Locate every blood parasite and identify its species.
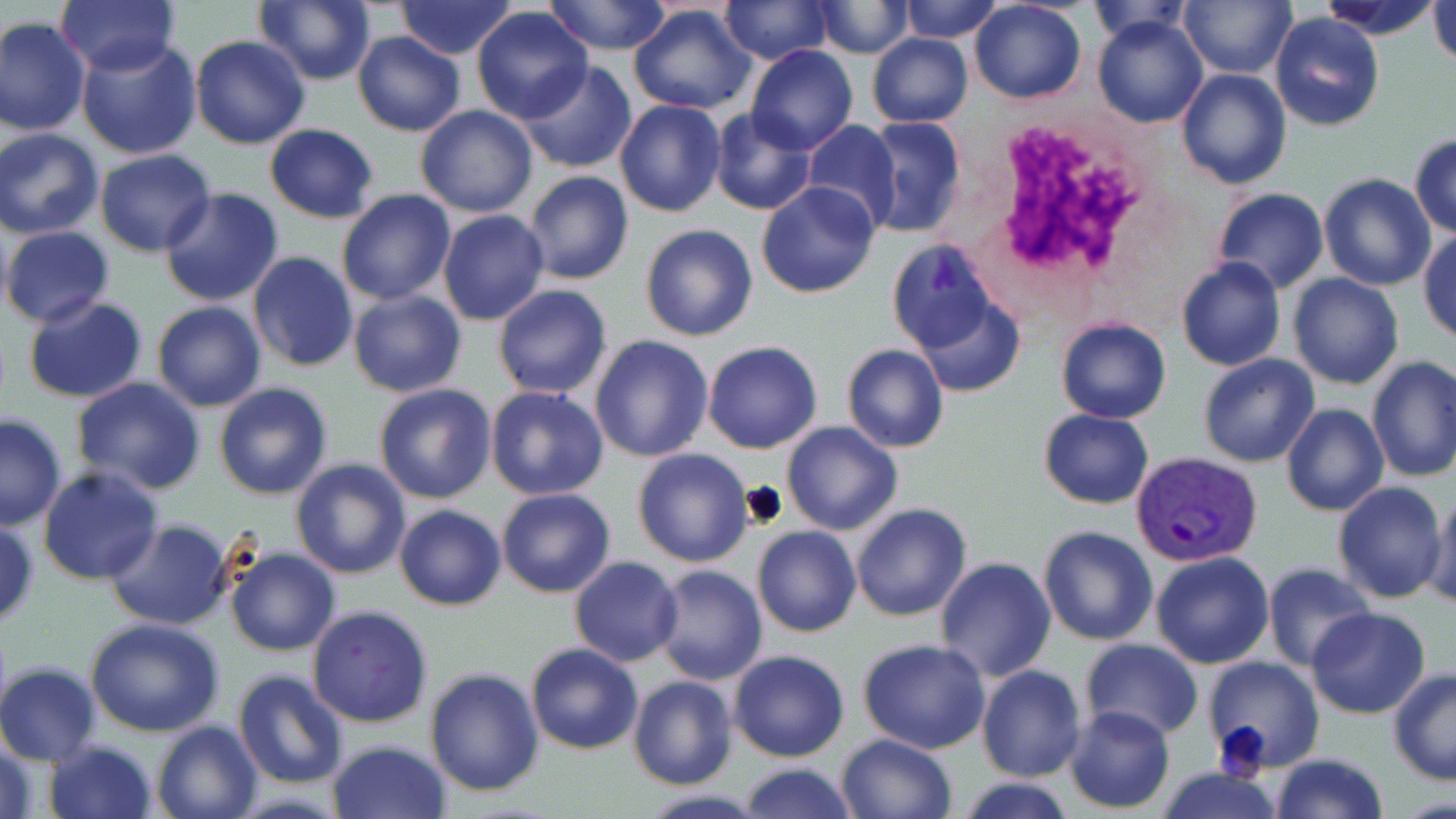
Approximate bounding boxes as (x1,y1)-(x2,y2) corner pairs in pixels.
Plasmodium vivax-infected red blood cells: (1131,452)-(1262,567).
No Plasmodium falciparum, Plasmodium ovale, Plasmodium malariae, Babesia divergens, or Trypanosoma brucei observed.

White blood cell locations: (979,118)-(1162,297). Uninfected red blood cell locations: (56,0)-(180,75), (255,0)-(376,86), (395,0)-(518,60), (543,0)-(673,55), (899,0)-(1004,42), (1085,0)-(1193,45), (1179,0)-(1295,78), (1321,0)-(1440,37), (1427,0)-(1456,67), (720,1)-(834,65), (811,1)-(914,59), (969,3)-(1087,105), (628,4)-(755,115), (471,8)-(594,124), (1270,11)-(1385,131), (1092,14)-(1209,129), (0,16)-(91,138), (353,31)-(466,138), (866,32)-(973,126), (76,34)-(203,159), (189,36)-(310,150), (747,46)-(858,154), (513,61)-(638,173), (1175,68)-(1291,190), (433,74)-(636,199), (613,100)-(727,218), (415,105)-(539,217), (708,107)-(816,216), (860,117)-(966,238), (799,120)-(901,230), (264,124)-(380,222), (1,128)-(104,238), (1409,134)-(1456,237), (94,150)-(216,256), (523,171)-(634,286), (1318,174)-(1437,292), (756,182)-(881,298), (159,187)-(284,307), (1211,189)-(1328,294), (336,191)-(456,306), (438,209)-(550,326), (641,224)-(758,342), (1,226)-(116,328), (1418,230)-(1456,343), (887,239)-(1009,362), (248,252)-(359,373), (1177,256)-(1287,372), (1287,274)-(1403,390), (493,284)-(613,400), (906,288)-(1024,397), (347,289)-(468,399), (22,296)-(148,404), (152,301)-(267,412), (1055,316)-(1172,423), (589,335)-(714,463), (702,341)-(822,454), (841,344)-(950,453), (1197,353)-(1321,467), (1366,357)-(1456,482), (69,378)-(207,495), (373,381)-(498,504), (214,382)-(334,500), (485,385)-(609,500), (1281,403)-(1389,516), (1038,409)-(1155,509), (0,412)-(66,532), (782,419)-(903,536), (633,447)-(754,567), (290,458)-(412,579), (38,466)-(165,586), (1333,481)-(1448,604), (1425,487)-(1455,611), (497,488)-(616,598), (851,503)-(972,621), (394,504)-(506,611), (104,518)-(235,630), (0,521)-(38,630), (1038,525)-(1159,646), (753,526)-(861,638), (226,546)-(340,656), (1150,551)-(1274,669), (570,557)-(683,666), (934,558)-(1056,681), (1262,563)-(1377,672), (650,566)-(768,685), (307,605)-(433,729), (1306,607)-(1431,720), (83,618)-(226,736), (858,639)-(990,753), (1079,639)-(1202,742), (525,642)-(643,755), (728,649)-(849,763), (1203,656)-(1322,771), (1,662)-(101,765), (976,665)-(1086,782), (1388,668)-(1456,785), (425,669)-(545,795), (233,671)-(348,789), (628,675)-(737,790), (1064,704)-(1177,814), (151,719)-(262,819), (835,734)-(957,819), (1,737)-(41,818), (43,739)-(158,818), (328,740)-(450,819), (1269,752)-(1388,819), (736,763)-(858,818), (1154,765)-(1285,819), (956,776)-(1078,818), (631,789)-(775,819). Slide-level diagnosis: Plasmodium vivax. May-Grünwald-Giemsa-stained preparation. One field of a larger specimen. Image is 1456×819 pixels. 1000x magnification. Light microscopy. Thin blood smear.